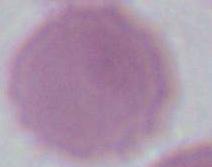

1000x magnification. Micrograph. A red blood cell is shown.